Locate every blood parasite and identify its species.
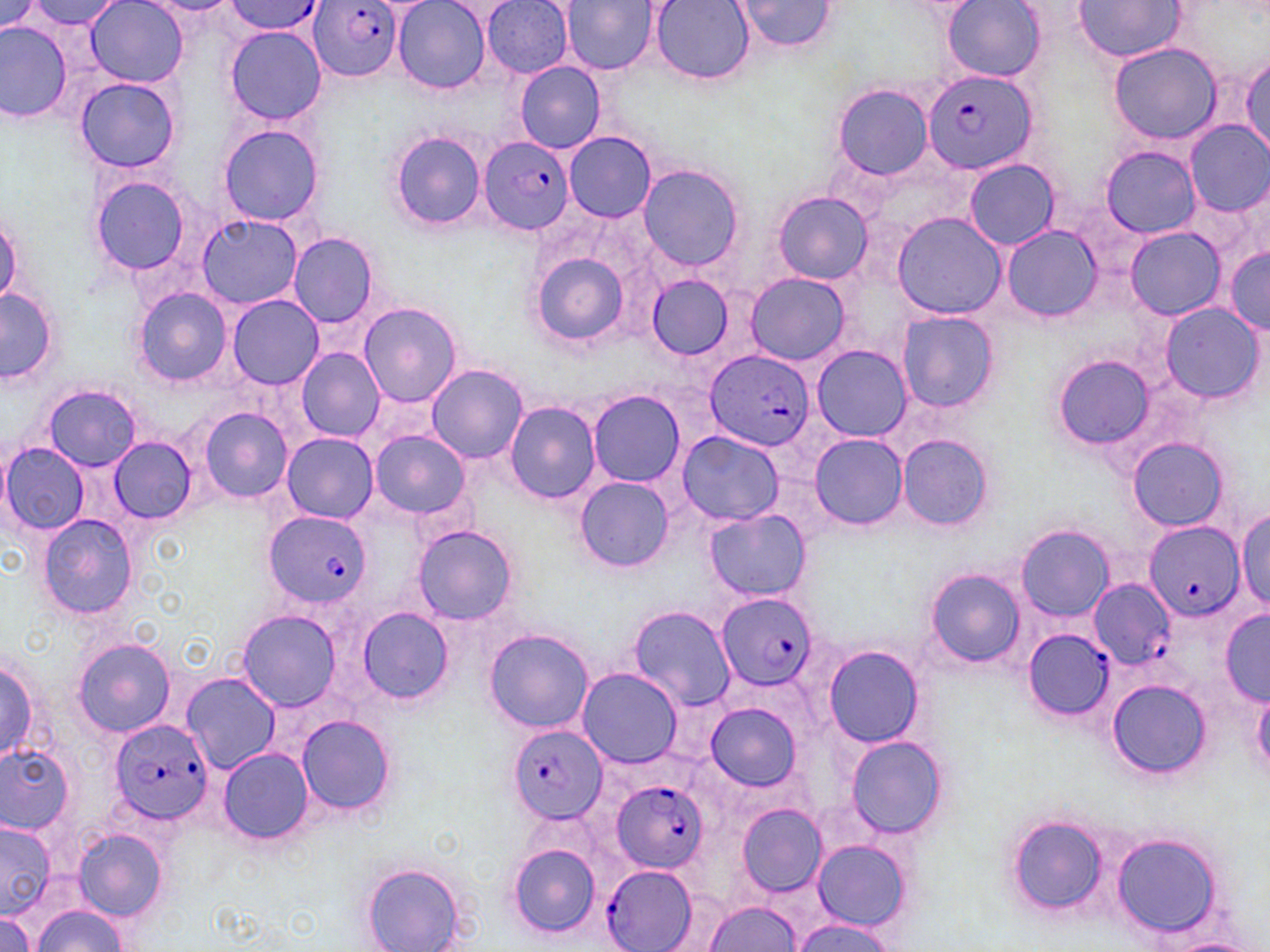
Approximate bounding boxes as named x1/y1/x2/y2 corners in pixels.
Plasmodium falciparum-infected red blood cells: (x1=307, y1=1, x2=405, y2=82), (x1=221, y1=2, x2=327, y2=35), (x1=922, y1=67, x2=1037, y2=175), (x1=479, y1=135, x2=576, y2=234), (x1=704, y1=350, x2=816, y2=454), (x1=264, y1=512, x2=370, y2=608), (x1=1144, y1=523, x2=1242, y2=622), (x1=1090, y1=579, x2=1172, y2=669), (x1=717, y1=593, x2=820, y2=689), (x1=1023, y1=628, x2=1113, y2=721), (x1=108, y1=719, x2=213, y2=824), (x1=509, y1=723, x2=607, y2=825), (x1=612, y1=779, x2=708, y2=873), (x1=601, y1=864, x2=699, y2=952).
No Plasmodium ovale, Plasmodium malariae, Plasmodium vivax, Babesia divergens, or Trypanosoma brucei observed.

Summary:
  - Uninfected red blood cell locations: (x1=28, y1=0, x2=123, y2=30), (x1=544, y1=0, x2=647, y2=124), (x1=650, y1=0, x2=754, y2=84), (x1=734, y1=0, x2=837, y2=54), (x1=0, y1=1, x2=45, y2=35), (x1=86, y1=1, x2=187, y2=86), (x1=392, y1=1, x2=492, y2=94), (x1=482, y1=1, x2=574, y2=77), (x1=562, y1=1, x2=658, y2=74), (x1=943, y1=1, x2=1043, y2=81), (x1=1073, y1=1, x2=1185, y2=62), (x1=0, y1=20, x2=71, y2=123), (x1=225, y1=26, x2=327, y2=125), (x1=1106, y1=40, x2=1226, y2=144), (x1=1240, y1=55, x2=1270, y2=158), (x1=514, y1=61, x2=606, y2=153), (x1=74, y1=76, x2=181, y2=173), (x1=832, y1=84, x2=935, y2=180), (x1=1186, y1=121, x2=1270, y2=215), (x1=218, y1=123, x2=324, y2=227), (x1=390, y1=130, x2=486, y2=231), (x1=564, y1=132, x2=656, y2=223), (x1=1102, y1=147, x2=1200, y2=238), (x1=963, y1=158, x2=1060, y2=251), (x1=636, y1=163, x2=747, y2=273), (x1=88, y1=174, x2=197, y2=278), (x1=773, y1=191, x2=872, y2=284), (x1=892, y1=212, x2=1006, y2=319), (x1=0, y1=213, x2=23, y2=308), (x1=196, y1=214, x2=303, y2=309), (x1=1002, y1=225, x2=1102, y2=322), (x1=1123, y1=228, x2=1228, y2=320), (x1=287, y1=232, x2=382, y2=329), (x1=1224, y1=247, x2=1270, y2=333), (x1=531, y1=251, x2=630, y2=345), (x1=744, y1=271, x2=852, y2=366), (x1=645, y1=274, x2=736, y2=361), (x1=0, y1=287, x2=59, y2=386), (x1=132, y1=288, x2=233, y2=387), (x1=228, y1=295, x2=321, y2=388), (x1=359, y1=302, x2=461, y2=407), (x1=1159, y1=303, x2=1265, y2=404), (x1=895, y1=310, x2=998, y2=413), (x1=811, y1=345, x2=912, y2=441), (x1=295, y1=347, x2=384, y2=441), (x1=1052, y1=354, x2=1154, y2=449), (x1=427, y1=364, x2=529, y2=464), (x1=43, y1=384, x2=142, y2=471), (x1=588, y1=388, x2=686, y2=487), (x1=503, y1=401, x2=602, y2=503), (x1=198, y1=406, x2=294, y2=502), (x1=369, y1=429, x2=470, y2=519), (x1=676, y1=431, x2=784, y2=525), (x1=896, y1=433, x2=994, y2=533), (x1=281, y1=434, x2=376, y2=523), (x1=809, y1=435, x2=909, y2=531), (x1=109, y1=436, x2=197, y2=524), (x1=1128, y1=437, x2=1232, y2=531), (x1=0, y1=441, x2=90, y2=536), (x1=577, y1=476, x2=676, y2=572), (x1=1236, y1=507, x2=1269, y2=610), (x1=703, y1=509, x2=810, y2=601), (x1=38, y1=515, x2=138, y2=618), (x1=1015, y1=524, x2=1114, y2=621), (x1=414, y1=525, x2=518, y2=626), (x1=924, y1=567, x2=1025, y2=669), (x1=629, y1=606, x2=736, y2=710), (x1=358, y1=607, x2=452, y2=705), (x1=237, y1=609, x2=344, y2=712), (x1=1220, y1=610, x2=1269, y2=704), (x1=484, y1=628, x2=595, y2=733), (x1=73, y1=638, x2=176, y2=738), (x1=822, y1=646, x2=923, y2=748), (x1=0, y1=656, x2=42, y2=765), (x1=577, y1=668, x2=681, y2=769), (x1=182, y1=671, x2=279, y2=773), (x1=1106, y1=678, x2=1211, y2=779), (x1=1251, y1=687, x2=1270, y2=776), (x1=707, y1=702, x2=802, y2=791), (x1=296, y1=713, x2=397, y2=818), (x1=845, y1=737, x2=947, y2=839), (x1=0, y1=745, x2=76, y2=833), (x1=217, y1=747, x2=314, y2=844), (x1=736, y1=802, x2=828, y2=897), (x1=1007, y1=815, x2=1107, y2=918), (x1=0, y1=820, x2=56, y2=918), (x1=72, y1=828, x2=168, y2=922), (x1=1110, y1=834, x2=1225, y2=936), (x1=810, y1=836, x2=914, y2=933), (x1=506, y1=843, x2=602, y2=939), (x1=361, y1=863, x2=468, y2=952), (x1=704, y1=901, x2=802, y2=951), (x1=31, y1=905, x2=128, y2=951), (x1=0, y1=910, x2=38, y2=952), (x1=792, y1=919, x2=902, y2=950), (x1=1159, y1=938, x2=1262, y2=952)
  - Slide-level diagnosis: Plasmodium falciparum
  - Magnification: 1000x
  - Modality: optical microscopy
  - Preparation: thin blood film
  - Field of view: single
  - Image size: 1270×952 pixels
  - Stain: May-Grünwald-Giemsa